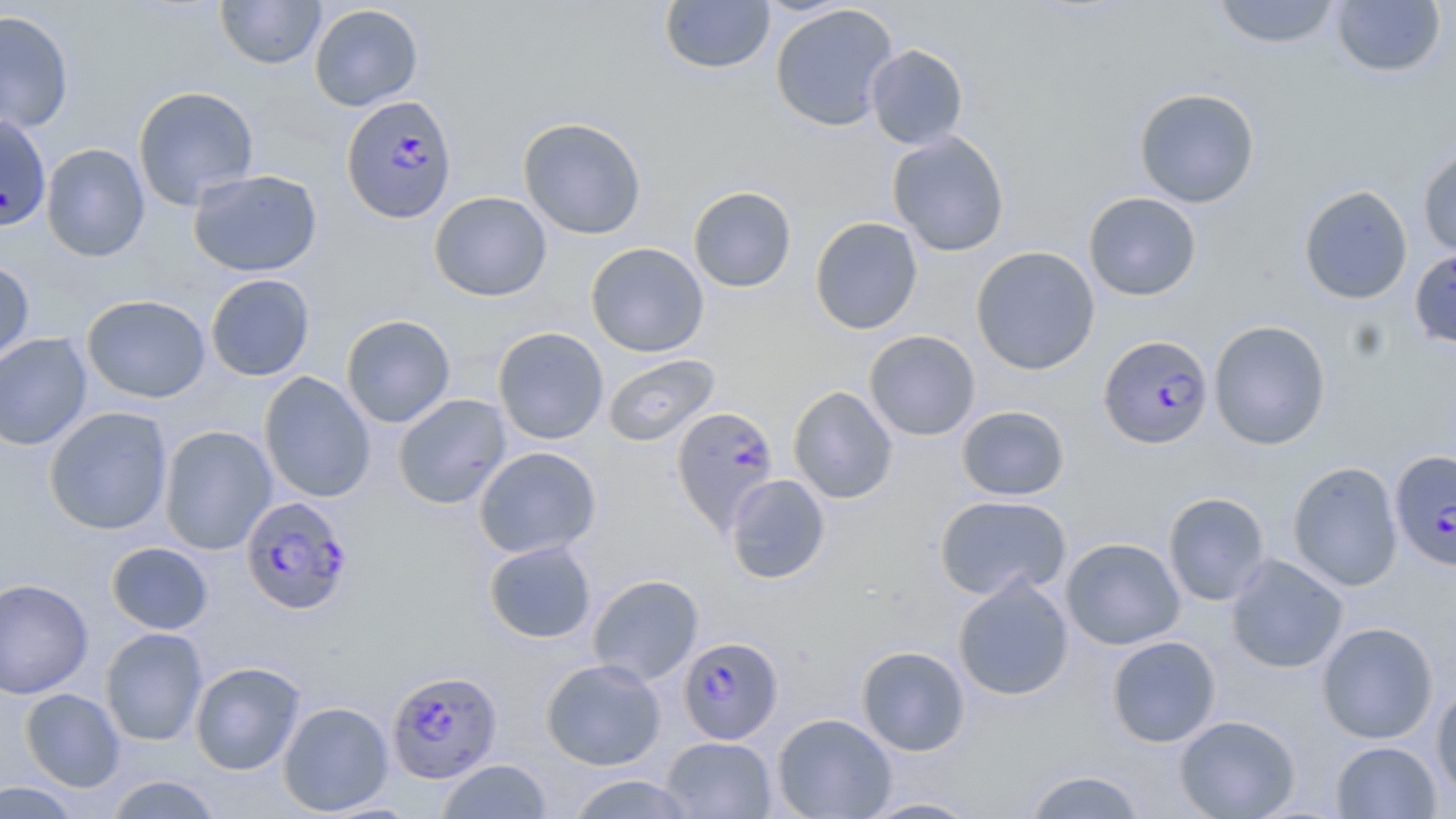

slide-level diagnosis = Plasmodium falciparum
image size = 1456×819 pixels
stain = May-Grünwald-Giemsa
preparation = thin blood film
magnification = 1000x
uninfected red blood cell locations = approximate bounding boxes as (x1,y1)-(x2,y2) corner pairs in pixels: (215,0)-(326,69), (659,0)-(775,75), (1211,0)-(1343,49), (1330,1)-(1447,78), (770,3)-(898,131), (309,4)-(424,111), (0,10)-(75,135), (866,44)-(969,150), (132,85)-(260,210), (1133,87)-(1260,207), (0,113)-(52,232), (518,117)-(646,240), (887,131)-(1010,257), (41,143)-(151,262), (1417,144)-(1456,259), (188,168)-(323,278), (1298,184)-(1413,305), (688,186)-(797,293), (429,191)-(553,302), (1083,192)-(1202,301), (810,216)-(923,334), (585,242)-(709,357), (971,245)-(1100,376), (1409,247)-(1456,348), (0,260)-(35,367), (205,273)-(315,381), (82,294)-(211,404), (341,314)-(456,428), (1208,320)-(1331,450), (493,326)-(609,444), (864,329)-(980,441), (0,332)-(92,451), (602,354)-(720,447), (259,372)-(376,503), (788,386)-(898,504), (393,393)-(511,509), (956,405)-(1070,501), (43,407)-(173,535), (158,425)-(277,555), (473,446)-(601,559), (1287,461)-(1403,591), (725,474)-(830,584), (1163,492)-(1271,605), (934,494)-(1072,601), (1060,537)-(1186,650), (483,540)-(597,644), (106,542)-(214,635), (1224,553)-(1348,674), (587,574)-(704,686), (952,576)-(1074,701), (0,578)-(93,699), (1316,622)-(1438,743), (100,627)-(208,745), (1106,635)-(1221,747), (856,645)-(970,756), (541,658)-(666,771), (190,661)-(307,775), (1431,683)-(1456,800), (20,688)-(125,792), (278,701)-(394,815), (772,713)-(897,818), (1174,715)-(1300,819), (660,736)-(777,818), (1331,741)-(1441,818), (436,759)-(553,818), (1021,769)-(1148,818), (564,773)-(697,818), (104,774)-(223,818), (0,781)-(84,818), (857,796)-(987,818)
field of view = single
modality = optical microscopy
Plasmodium falciparum-infected red blood cell locations = approximate bounding boxes as (x1,y1)-(x2,y2) corner pairs in pixels: (341,94)-(458,222), (1099,334)-(1213,449), (675,411)-(784,539), (1389,449)-(1456,571), (240,495)-(353,616), (678,636)-(783,744), (386,669)-(503,783)